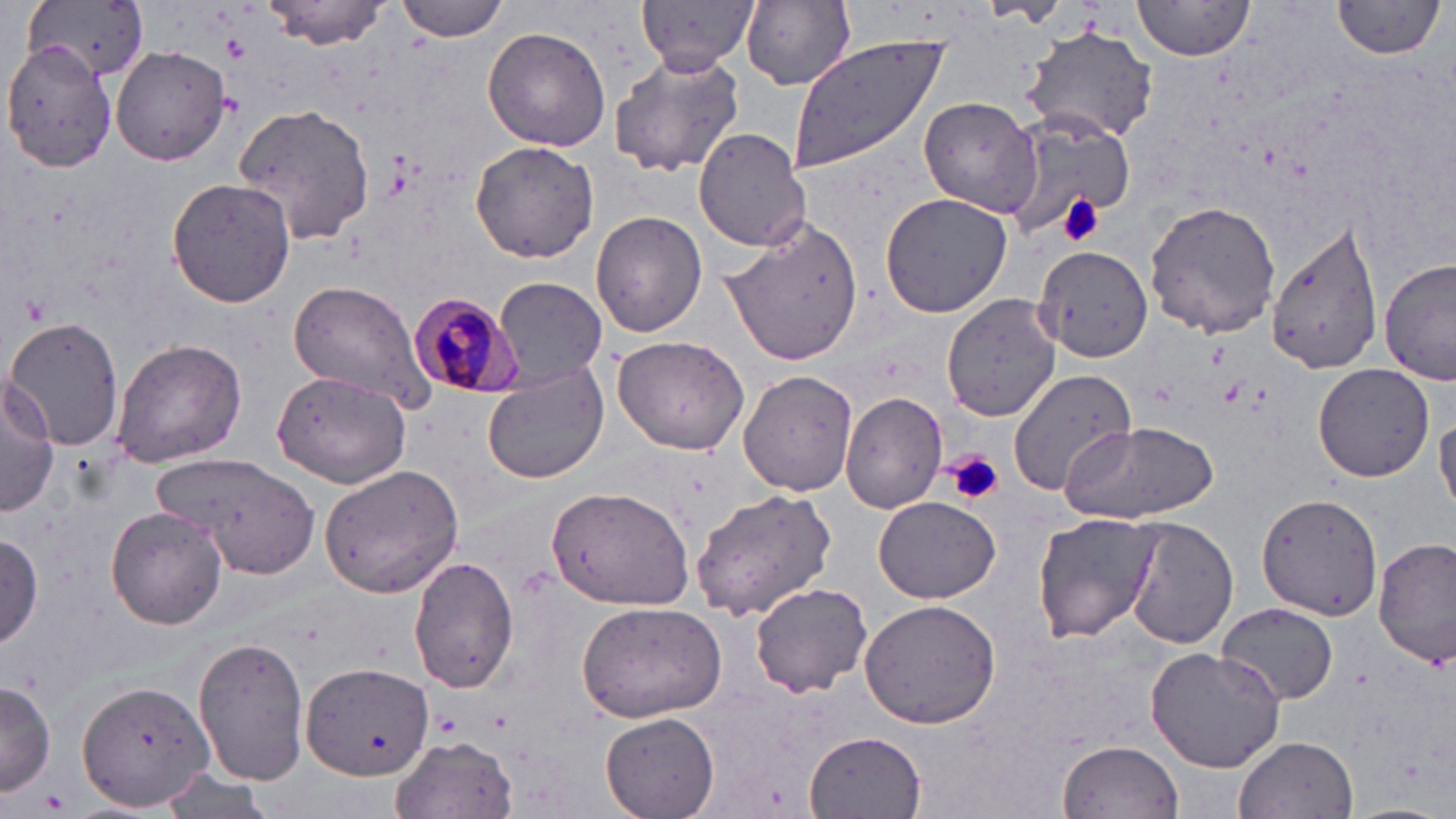

Approximate bounding boxes as (x1,y1)-(x2,y2) corner pairs in pixels. Uninfected red blood cell locations: (25,0)-(149,82), (397,0)-(511,40), (638,0)-(756,69), (741,0)-(858,90), (1131,0)-(1256,67), (261,1)-(396,49), (1331,1)-(1446,61), (981,2)-(1069,25), (1020,23)-(1159,145), (484,26)-(612,151), (788,32)-(951,174), (3,40)-(119,172), (112,45)-(231,166), (610,53)-(745,179), (918,97)-(1041,215), (229,100)-(373,249), (999,107)-(1137,237), (693,128)-(810,252), (470,141)-(599,264), (166,178)-(296,307), (880,192)-(1012,318), (1143,200)-(1281,339), (592,211)-(707,338), (722,215)-(863,367), (1268,217)-(1385,376), (1033,244)-(1153,362), (1380,257)-(1455,387), (494,276)-(606,388), (288,280)-(435,412), (941,293)-(1064,423), (6,315)-(124,451), (612,336)-(751,457), (111,337)-(247,467), (1313,362)-(1435,481), (482,364)-(609,484), (1006,365)-(1139,500), (739,368)-(858,497), (273,371)-(411,488), (0,373)-(61,514), (840,391)-(951,513), (1435,417)-(1456,517), (1061,420)-(1220,524), (154,453)-(320,576), (319,463)-(467,596), (546,483)-(698,612), (691,488)-(838,618), (1256,492)-(1384,621), (873,495)-(1000,604), (106,507)-(227,629), (1033,513)-(1162,646), (1125,518)-(1236,650), (0,532)-(44,649), (1374,539)-(1455,667), (410,558)-(520,693), (750,581)-(875,698), (858,599)-(1002,728), (575,600)-(727,722), (1217,602)-(1338,705), (192,633)-(308,785), (1144,646)-(1285,773), (301,661)-(434,781), (77,678)-(214,813), (0,679)-(55,798), (602,712)-(718,818), (806,731)-(926,818), (392,734)-(517,818), (1235,734)-(1358,819), (1059,740)-(1184,818), (158,765)-(275,816). Platelet locations: (221,33)-(250,62), (1057,194)-(1101,246), (947,450)-(1004,506). Plasmodium malariae-infected red blood cell locations: (409,292)-(523,400). Slide-level diagnosis: Plasmodium malariae. Image is 1456×819 pixels. Optical microscopy. Thin blood smear. Single field of view. Captured at 1000x magnification. May-Grünwald-Giemsa-stained preparation.